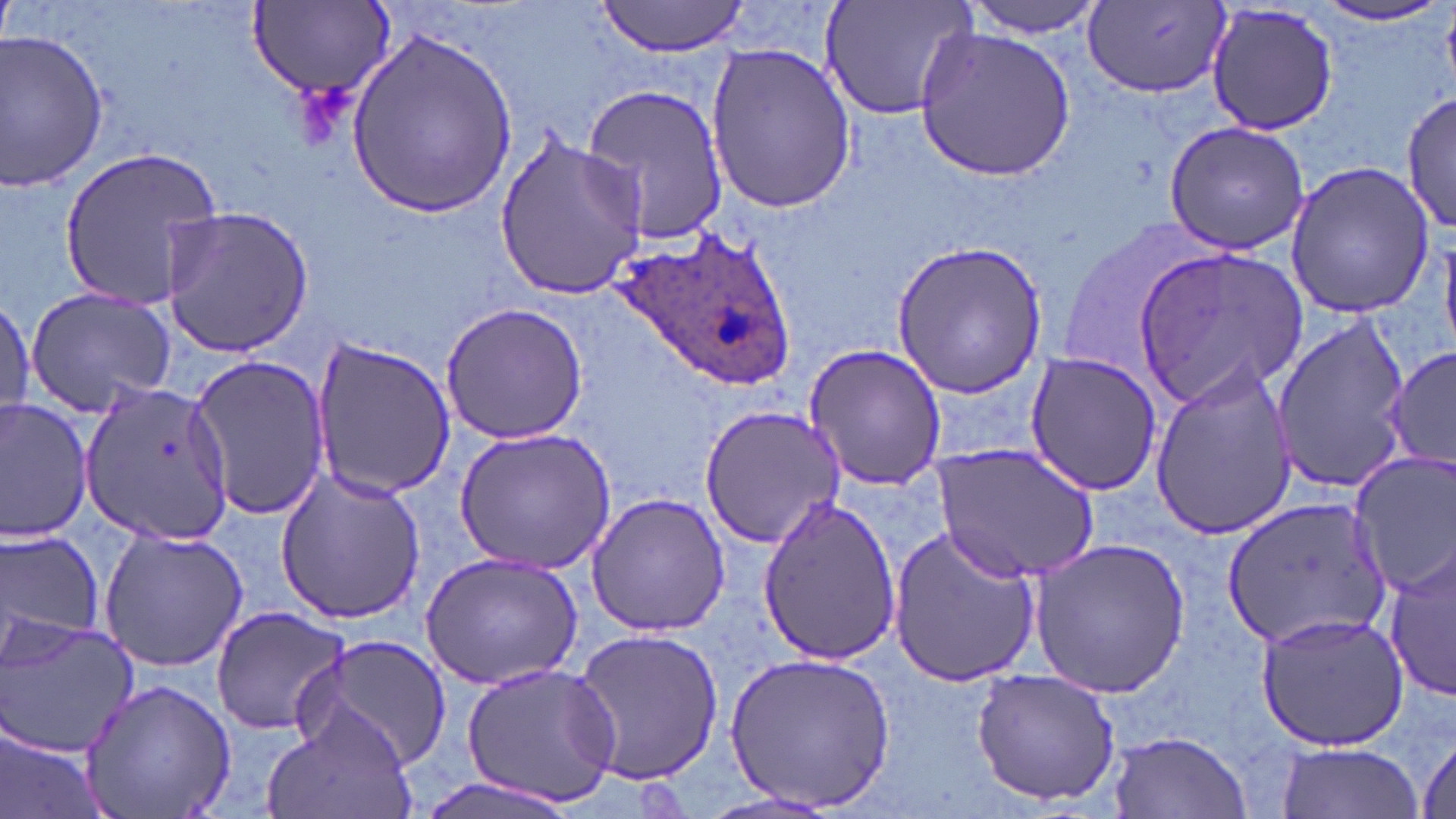

slide-level diagnosis = Plasmodium ovale
magnification = 1000x
uninfected red blood cell locations = approximate bounding boxes as named x1/y1/x2/y2 corners in pixels: (x1=818, y1=0, x2=979, y2=123), (x1=961, y1=0, x2=1109, y2=37), (x1=595, y1=1, x2=752, y2=57), (x1=248, y1=3, x2=396, y2=104), (x1=1081, y1=3, x2=1229, y2=96), (x1=1205, y1=3, x2=1340, y2=138), (x1=1307, y1=3, x2=1451, y2=27), (x1=915, y1=27, x2=1076, y2=179), (x1=0, y1=29, x2=110, y2=189), (x1=346, y1=32, x2=517, y2=219), (x1=703, y1=41, x2=855, y2=213), (x1=581, y1=83, x2=730, y2=246), (x1=1403, y1=90, x2=1454, y2=234), (x1=1161, y1=119, x2=1313, y2=256), (x1=491, y1=132, x2=652, y2=300), (x1=58, y1=144, x2=226, y2=316), (x1=1282, y1=160, x2=1433, y2=317), (x1=157, y1=205, x2=315, y2=357), (x1=892, y1=240, x2=1050, y2=398), (x1=1137, y1=246, x2=1310, y2=407), (x1=25, y1=285, x2=179, y2=417), (x1=0, y1=292, x2=35, y2=422), (x1=441, y1=303, x2=590, y2=445), (x1=1270, y1=317, x2=1414, y2=489), (x1=307, y1=335, x2=456, y2=504), (x1=804, y1=344, x2=947, y2=493), (x1=1386, y1=347, x2=1455, y2=466), (x1=1023, y1=351, x2=1164, y2=496), (x1=187, y1=354, x2=333, y2=523), (x1=1148, y1=361, x2=1298, y2=540), (x1=80, y1=386, x2=235, y2=545), (x1=0, y1=398, x2=93, y2=543), (x1=698, y1=401, x2=845, y2=550), (x1=453, y1=429, x2=615, y2=576), (x1=933, y1=443, x2=1098, y2=582), (x1=1349, y1=451, x2=1456, y2=597), (x1=274, y1=466, x2=426, y2=627), (x1=586, y1=493, x2=731, y2=637), (x1=755, y1=497, x2=904, y2=666), (x1=1220, y1=499, x2=1389, y2=652), (x1=887, y1=524, x2=1042, y2=687), (x1=0, y1=528, x2=104, y2=658), (x1=98, y1=528, x2=250, y2=672), (x1=1029, y1=538, x2=1191, y2=698), (x1=1386, y1=548, x2=1456, y2=704), (x1=418, y1=549, x2=587, y2=692), (x1=208, y1=605, x2=354, y2=736), (x1=1255, y1=612, x2=1411, y2=750), (x1=0, y1=615, x2=140, y2=758), (x1=572, y1=627, x2=724, y2=785), (x1=296, y1=635, x2=453, y2=771), (x1=723, y1=648, x2=900, y2=814), (x1=460, y1=659, x2=619, y2=808), (x1=970, y1=668, x2=1121, y2=807), (x1=80, y1=680, x2=237, y2=818), (x1=263, y1=704, x2=419, y2=819), (x1=0, y1=726, x2=112, y2=819), (x1=1108, y1=731, x2=1252, y2=816), (x1=1415, y1=731, x2=1456, y2=816), (x1=1276, y1=742, x2=1426, y2=819), (x1=411, y1=773, x2=581, y2=819), (x1=701, y1=789, x2=847, y2=819)
preparation = thin blood smear
modality = light microscopy
image size = 1456×819 pixels
stain = May-Grünwald-Giemsa
field of view = single
Plasmodium ovale-infected red blood cell locations = approximate bounding boxes as named x1/y1/x2/y2 corners in pixels: (x1=615, y1=225, x2=798, y2=391)